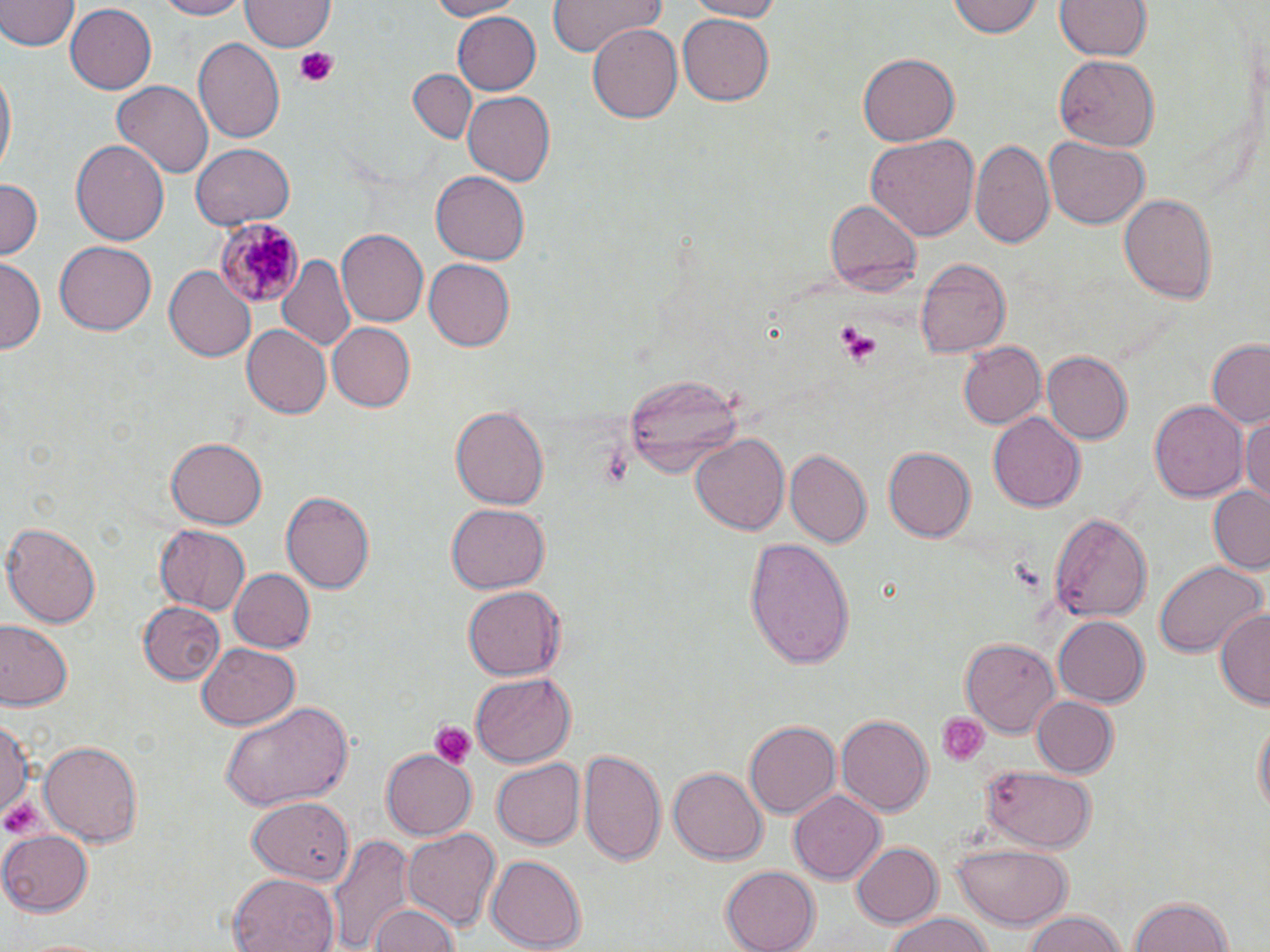
{
  "slide_level_diagnosis": "Plasmodium malariae",
  "stain": "May-Grünwald-Giemsa",
  "magnification": "1000x",
  "field_of_view": "single",
  "image_size": "1270×952 pixels",
  "platelet_locations": "approximate bounding boxes as (x1,y1)-(x2,y2) corner pairs in pixels: (291,46)-(342,87), (832,323)-(880,364), (601,447)-(633,491), (936,712)-(991,768), (427,721)-(477,768), (1,797)-(53,841)",
  "modality": "light microscopy",
  "plasmodium_malariae_infected_red_blood_cell_locations": "approximate bounding boxes as (x1,y1)-(x2,y2) corner pairs in pixels: (213,219)-(304,308)",
  "preparation": "thin blood smear",
  "uninfected_red_blood_cell_locations": "approximate bounding boxes as (x1,y1)-(x2,y2) corner pairs in pixels: (150,0)-(250,19), (419,0)-(523,21), (545,0)-(665,57), (684,0)-(789,21), (948,0)-(1043,40), (0,1)-(78,53), (1054,1)-(1152,63), (239,2)-(332,52), (64,5)-(157,92), (453,10)-(542,94), (677,11)-(773,104), (588,22)-(687,121), (194,36)-(285,144), (858,53)-(960,146), (1052,55)-(1160,151), (406,68)-(476,144), (0,69)-(15,181), (113,80)-(213,178), (463,90)-(556,187), (867,133)-(978,241), (70,137)-(169,244), (969,137)-(1054,248), (1045,137)-(1149,229), (190,143)-(295,228), (431,172)-(528,265), (0,178)-(42,264), (1119,192)-(1218,306), (825,198)-(922,296), (338,228)-(433,326), (56,241)-(156,337), (278,254)-(355,349), (423,257)-(514,350), (914,257)-(1009,357), (0,259)-(43,351), (165,265)-(256,362), (326,322)-(416,411), (242,323)-(334,418), (1206,339)-(1270,430), (958,341)-(1047,429), (1042,350)-(1133,444), (621,369)-(743,477), (1149,399)-(1248,504), (451,404)-(549,512), (988,412)-(1086,513), (1241,414)-(1270,508), (690,434)-(788,537), (166,437)-(266,528), (882,447)-(974,542), (786,451)-(871,548), (1208,485)-(1270,574), (281,491)-(375,595), (447,503)-(548,594), (1048,510)-(1152,622), (3,522)-(102,629), (153,526)-(251,614), (745,538)-(856,668), (1155,561)-(1263,659), (230,567)-(314,653), (462,585)-(565,681), (137,601)-(225,684), (1215,606)-(1270,712), (1053,616)-(1148,708), (2,623)-(74,709), (960,636)-(1060,738), (196,641)-(299,729), (472,672)-(577,767), (1030,695)-(1118,777), (217,699)-(357,812), (0,711)-(29,828), (835,714)-(931,815), (1251,716)-(1269,825), (743,719)-(840,820), (38,738)-(142,844), (581,747)-(668,869), (380,750)-(476,839), (490,759)-(585,848), (670,766)-(766,864), (980,766)-(1097,852), (788,790)-(884,886), (246,797)-(351,879), (404,827)-(501,933), (1,831)-(94,915), (331,832)-(413,952), (850,841)-(942,928), (951,844)-(1067,927), (485,855)-(584,950), (721,866)-(819,952), (228,874)-(339,952), (1127,895)-(1236,952), (370,905)-(462,952), (1017,909)-(1132,951), (879,913)-(999,952)"
}